State the blood parasite species.
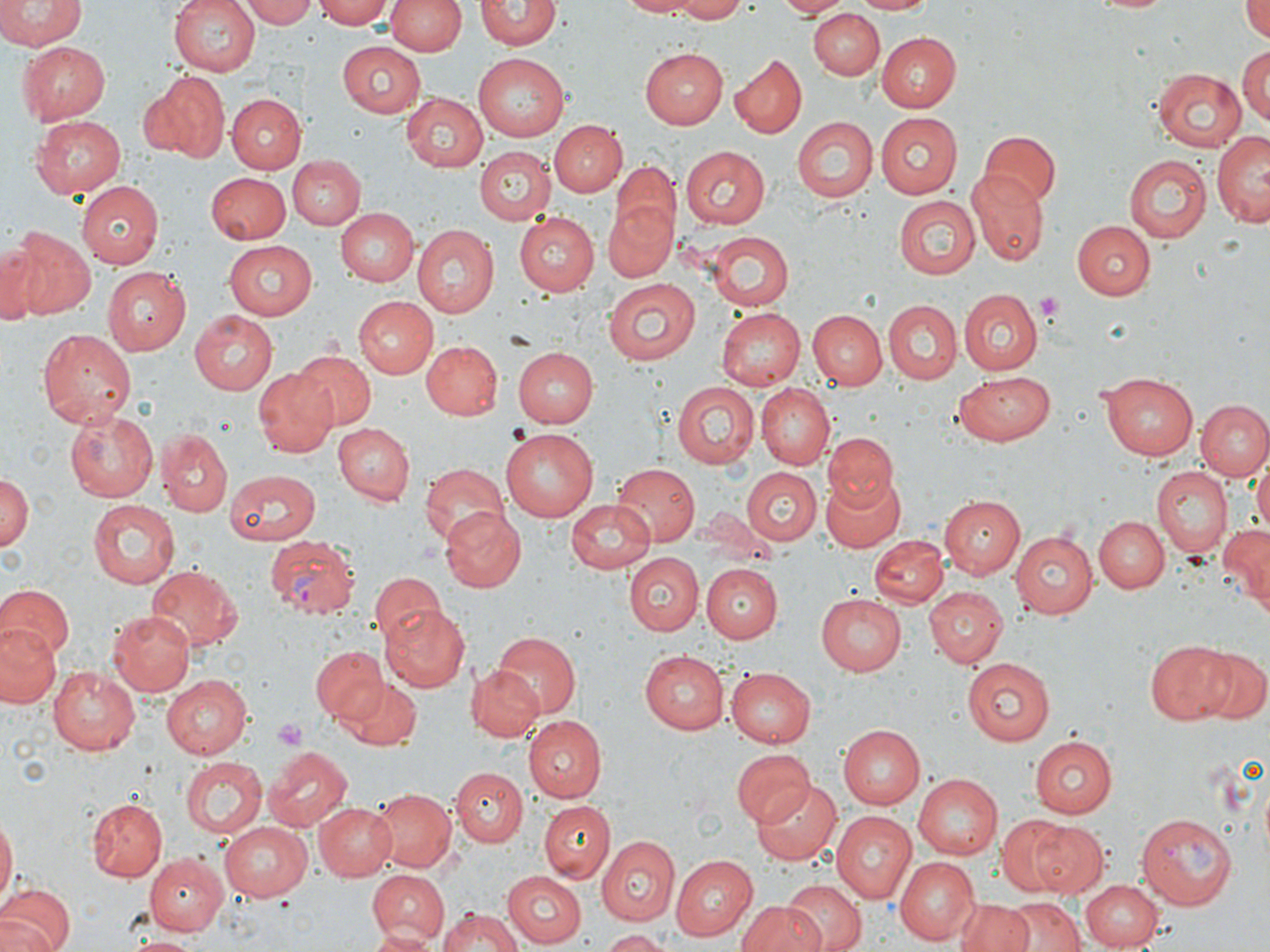

Plasmodium vivax.

Approximate bounding boxes as [x1, y1, x2, y2] in pixels. Platelet locations: [1034, 292, 1063, 324], [272, 717, 309, 750]. Uninfected red blood cell locations: [0, 0, 85, 51], [169, 0, 260, 76], [241, 0, 321, 28], [316, 0, 393, 28], [386, 0, 463, 57], [476, 0, 559, 51], [616, 0, 709, 17], [662, 0, 754, 22], [774, 0, 852, 17], [851, 0, 936, 15], [1083, 0, 1183, 15], [1243, 0, 1270, 42], [809, 6, 885, 79], [875, 31, 960, 111], [338, 42, 426, 118], [16, 43, 110, 123], [1238, 45, 1269, 127], [642, 47, 729, 129], [474, 54, 569, 141], [730, 55, 808, 139], [1151, 67, 1248, 152], [141, 72, 228, 160], [403, 91, 491, 172], [226, 94, 303, 173], [875, 113, 963, 199], [30, 116, 126, 198], [791, 116, 878, 203], [549, 120, 626, 197], [1213, 130, 1270, 227], [981, 131, 1060, 208], [474, 146, 555, 226], [680, 146, 770, 230], [615, 153, 752, 241], [1124, 155, 1210, 243], [285, 156, 364, 230], [610, 162, 681, 244], [205, 172, 289, 245], [967, 172, 1048, 264], [77, 180, 165, 267], [895, 197, 981, 278], [603, 200, 676, 281], [335, 207, 418, 287], [514, 213, 599, 295], [1073, 220, 1155, 299], [411, 225, 497, 316], [10, 228, 94, 320], [704, 231, 794, 311], [221, 239, 316, 319], [1, 240, 45, 324], [103, 267, 192, 354], [603, 277, 700, 365], [959, 290, 1041, 373], [354, 297, 436, 377], [885, 299, 963, 383], [713, 307, 806, 390], [189, 310, 277, 394], [808, 310, 888, 390], [37, 327, 136, 426], [421, 341, 502, 420], [515, 345, 597, 425], [292, 351, 374, 429], [253, 368, 337, 456], [952, 370, 1056, 447], [1100, 372, 1199, 459], [672, 381, 758, 466], [758, 384, 833, 466], [1197, 400, 1270, 481], [65, 408, 158, 502], [331, 423, 413, 506], [500, 428, 598, 521], [157, 429, 231, 515], [822, 433, 900, 510], [1250, 451, 1270, 541], [419, 462, 509, 549], [612, 463, 699, 547], [1151, 466, 1232, 561], [743, 468, 821, 546], [225, 470, 321, 545], [0, 471, 32, 554], [819, 474, 906, 553], [938, 496, 1025, 578], [564, 498, 656, 570], [87, 501, 178, 588], [440, 505, 525, 592], [699, 506, 771, 558], [1095, 514, 1170, 591], [1219, 524, 1270, 609], [1010, 529, 1099, 618], [870, 535, 948, 609], [625, 554, 702, 635], [147, 563, 240, 651], [701, 564, 782, 642], [371, 573, 446, 648], [1, 584, 73, 660], [923, 586, 1006, 667], [815, 593, 908, 675], [380, 603, 468, 691], [106, 608, 195, 696], [0, 623, 61, 706], [487, 632, 584, 717], [1145, 640, 1238, 725], [311, 644, 386, 721], [643, 649, 729, 733], [1194, 649, 1268, 725], [961, 657, 1056, 744], [46, 664, 141, 754], [465, 664, 542, 742], [725, 667, 816, 747], [161, 677, 253, 759], [337, 678, 422, 752], [521, 714, 606, 802], [838, 724, 926, 808], [1028, 734, 1118, 817], [265, 746, 353, 831], [730, 750, 812, 830], [182, 755, 265, 839], [451, 767, 526, 845], [912, 774, 1002, 859], [752, 779, 841, 865], [372, 787, 456, 871], [86, 798, 167, 880], [538, 800, 614, 882], [315, 801, 396, 880], [831, 811, 916, 904], [0, 816, 17, 904], [1011, 816, 1107, 897], [219, 822, 311, 900], [601, 836, 680, 926], [144, 852, 227, 936], [673, 854, 756, 940], [896, 855, 979, 943], [366, 870, 448, 943], [501, 872, 586, 947], [1080, 879, 1160, 949], [782, 880, 865, 952], [0, 883, 74, 952], [1003, 896, 1086, 952], [954, 898, 1034, 952], [735, 901, 827, 952], [436, 909, 527, 951], [365, 927, 438, 952], [599, 931, 668, 952], [124, 933, 203, 951]. Plasmodium vivax-infected red blood cell locations: [262, 535, 359, 618], [1135, 810, 1238, 908]. Thin blood smear. May-Grünwald-Giemsa stain. Captured at 1000x magnification. Image is 1270×952 pixels. Optical microscopy. One field of a larger specimen.